Assess the morphology of the red blood cells.
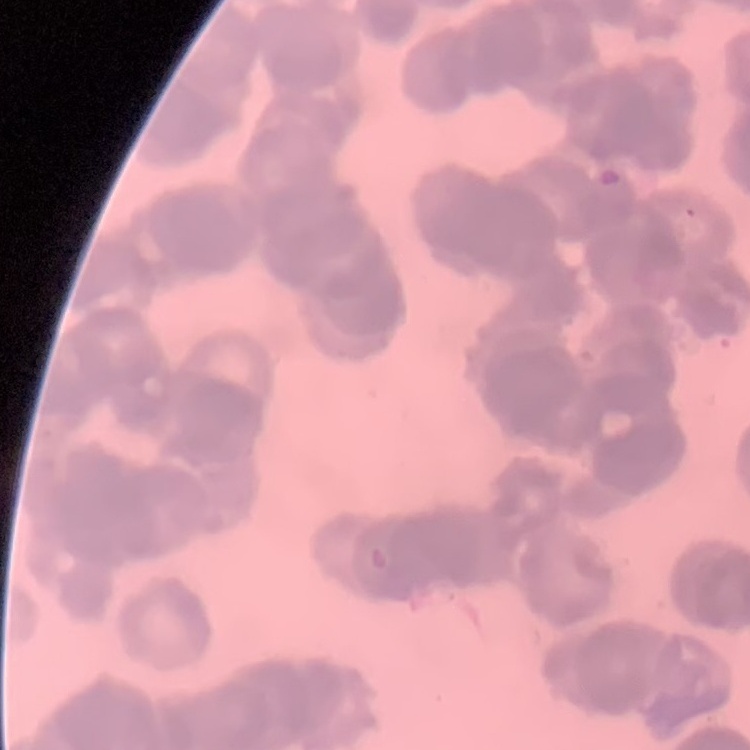

They show rouleaux formation.

Stained with either Field's or Giemsa. Thin peripheral smear. One tile cut from a larger photomicrograph.